Identify the parasite.
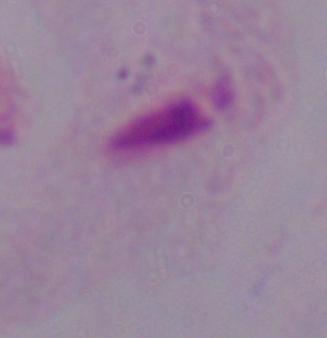
A trichomonad.

1000x magnification. Photomicrograph.